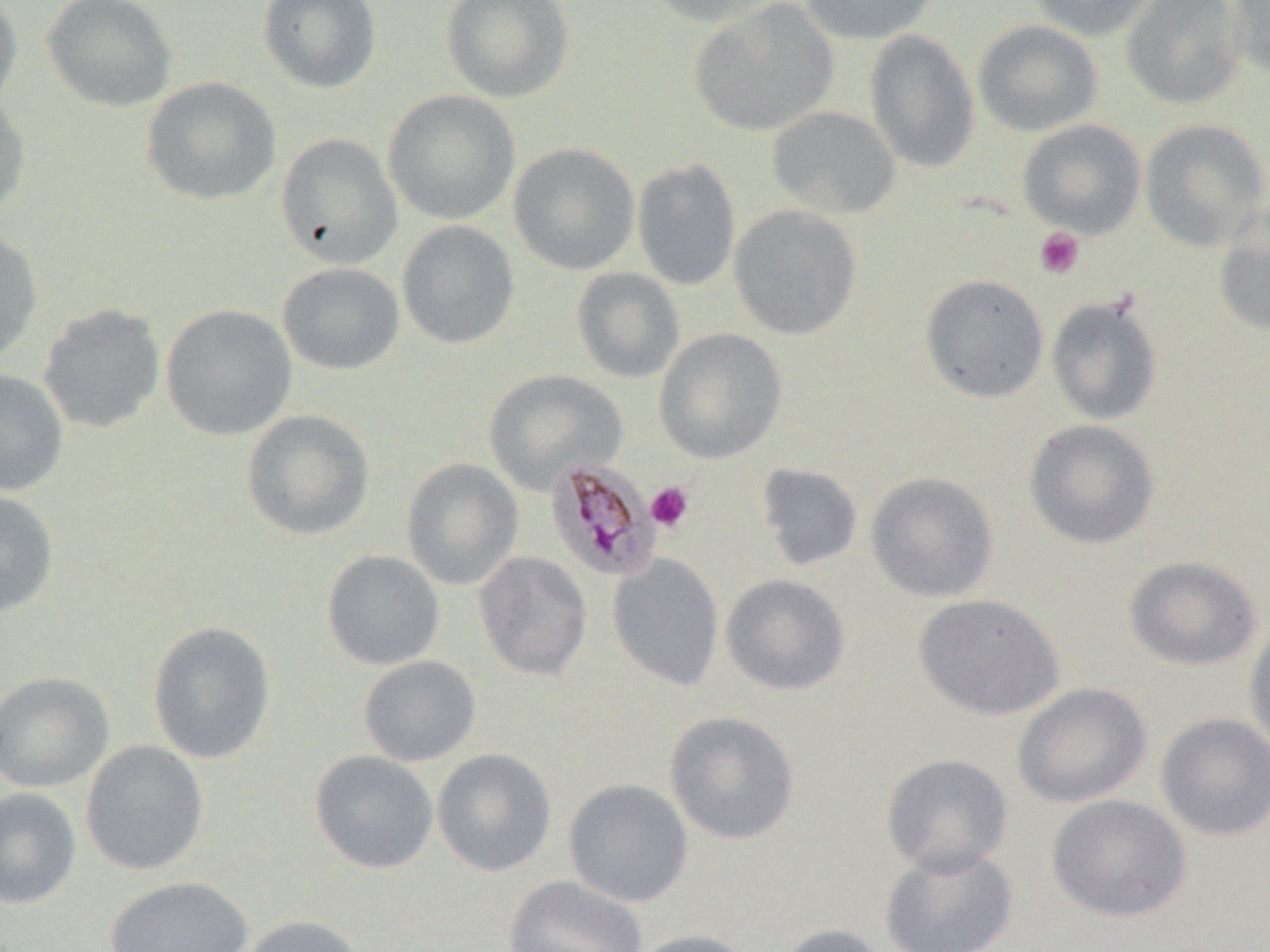
Approximate bounding boxes as [x1, y1, x2, y2] in pixels. Uninfected red blood cell locations: [0, 0, 23, 114], [41, 0, 178, 112], [258, 0, 382, 93], [441, 0, 574, 103], [644, 0, 786, 28], [799, 0, 939, 45], [1027, 0, 1159, 42], [1120, 0, 1246, 110], [1226, 0, 1270, 79], [689, 1, 839, 136], [972, 19, 1103, 137], [865, 28, 980, 172], [140, 76, 282, 206], [382, 89, 521, 226], [0, 93, 31, 219], [765, 105, 901, 219], [1139, 117, 1269, 250], [1017, 119, 1146, 239], [275, 133, 402, 269], [508, 142, 641, 275], [631, 157, 741, 291], [729, 204, 862, 340], [1213, 206, 1270, 337], [396, 220, 520, 349], [0, 230, 43, 363], [277, 262, 405, 375], [571, 267, 685, 384], [920, 273, 1049, 403], [1046, 295, 1163, 426], [37, 303, 166, 434], [160, 303, 297, 441], [653, 328, 787, 464], [0, 367, 69, 496], [483, 369, 628, 495], [241, 409, 375, 541], [1024, 419, 1160, 550], [401, 458, 524, 590], [756, 462, 864, 572], [865, 471, 999, 603], [0, 489, 59, 617], [322, 550, 445, 670], [473, 551, 592, 681], [607, 554, 724, 692], [1124, 555, 1263, 671], [720, 574, 851, 696], [913, 593, 1065, 721], [1245, 620, 1270, 759], [147, 621, 276, 764], [358, 655, 481, 766], [0, 671, 115, 793], [1012, 682, 1152, 808], [664, 710, 800, 845], [1155, 713, 1270, 841], [80, 739, 209, 875], [431, 748, 557, 877], [310, 750, 439, 874], [880, 753, 1013, 876], [563, 778, 694, 907], [0, 787, 82, 909], [1045, 794, 1192, 923], [878, 843, 1019, 952], [504, 875, 648, 952], [104, 876, 253, 952], [240, 914, 369, 952], [773, 924, 887, 952], [624, 928, 757, 952]. Plasmodium malariae-infected red blood cell locations: [544, 457, 660, 582]. Platelet locations: [1034, 227, 1084, 280], [645, 481, 694, 532]. Slide-level diagnosis: Plasmodium malariae. Light microscopy. 1000x magnification. One field of a larger specimen. Image is 1270×952 pixels. Thin blood film. May-Grünwald-Giemsa stain.